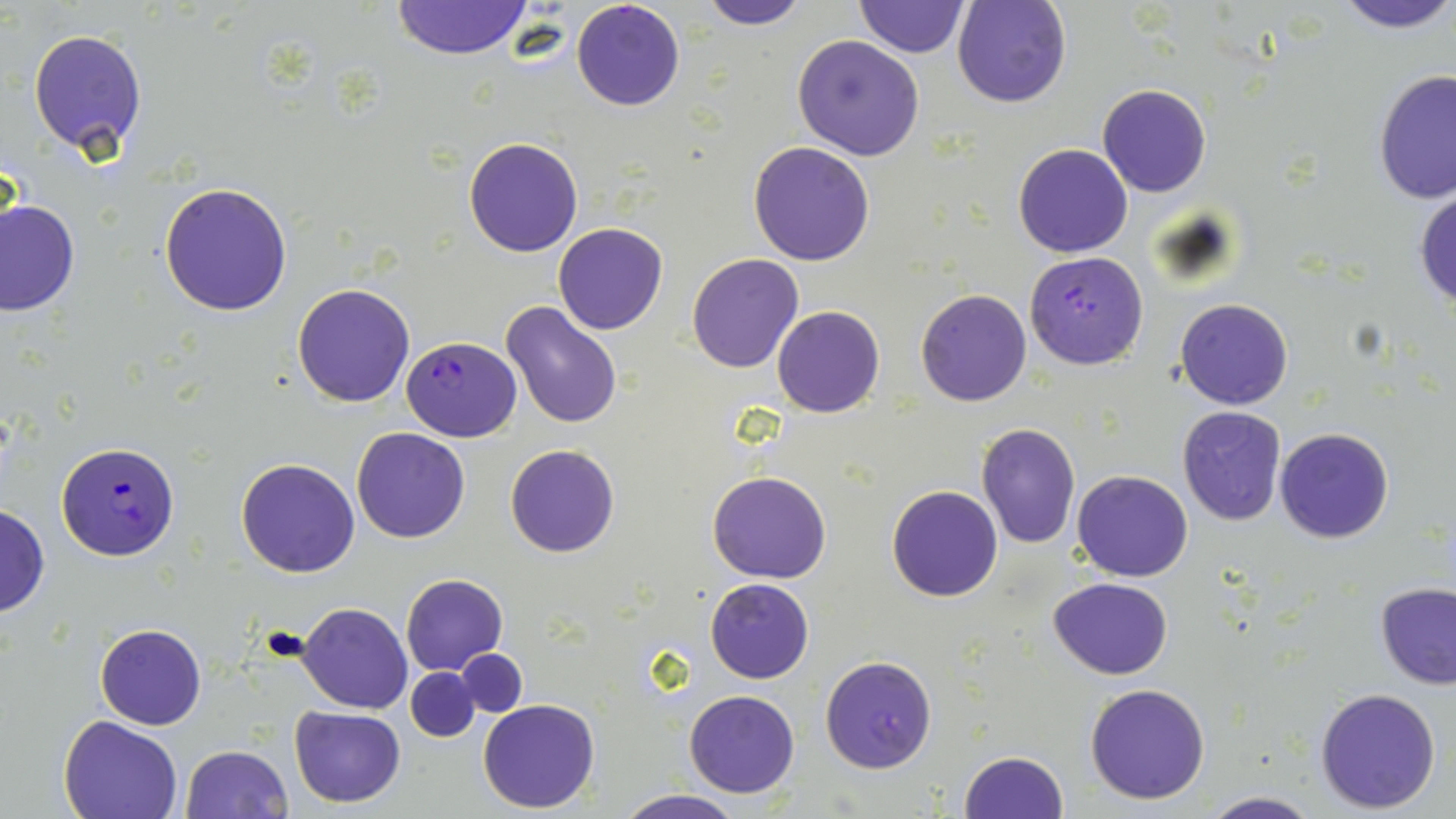

Summary:
  - Coordinate format: approximate bounding boxes as (x1,y1)-(x2,y2) corner pairs in pixels
  - Uninfected red blood cell locations: (695,0)-(811,29), (855,0)-(969,57), (1332,0)-(1455,34), (390,1)-(534,60), (951,1)-(1071,108), (27,28)-(148,157), (792,34)-(925,160), (1374,70)-(1456,207), (1097,84)-(1212,197), (463,137)-(583,256), (749,142)-(875,266), (1013,144)-(1133,258), (159,182)-(293,318), (1413,186)-(1456,309), (1,200)-(80,315), (552,222)-(669,335), (686,253)-(805,373), (292,283)-(415,407), (916,288)-(1031,406), (1174,298)-(1293,409), (499,299)-(623,430), (773,305)-(885,416), (1176,406)-(1288,527), (975,424)-(1081,549), (351,428)-(471,544), (1275,428)-(1393,544), (505,443)-(620,559), (237,457)-(361,577), (707,470)-(833,583), (1072,470)-(1194,581), (886,484)-(1003,602), (0,503)-(49,617), (400,573)-(508,676), (1048,576)-(1173,679), (706,578)-(814,683), (1375,581)-(1456,689), (298,601)-(412,714), (95,624)-(206,729), (455,650)-(527,716), (819,653)-(938,774), (405,667)-(480,742), (1085,682)-(1212,804), (1314,687)-(1442,813), (684,689)-(799,797), (478,698)-(600,813), (289,706)-(405,808), (60,717)-(183,819), (179,745)-(292,819), (959,749)-(1069,819), (615,790)-(746,819), (1199,791)-(1321,819)
  - Plasmodium falciparum-infected red blood cell locations: (570,0)-(686,112), (1025,251)-(1149,369), (402,336)-(522,441), (55,441)-(180,560)
  - Slide-level diagnosis: Plasmodium falciparum
  - Modality: light microscopy
  - Image size: 1456×819 pixels
  - Preparation: thin blood smear
  - Stain: May-Grünwald-Giemsa
  - Field of view: single
  - Magnification: 1000x